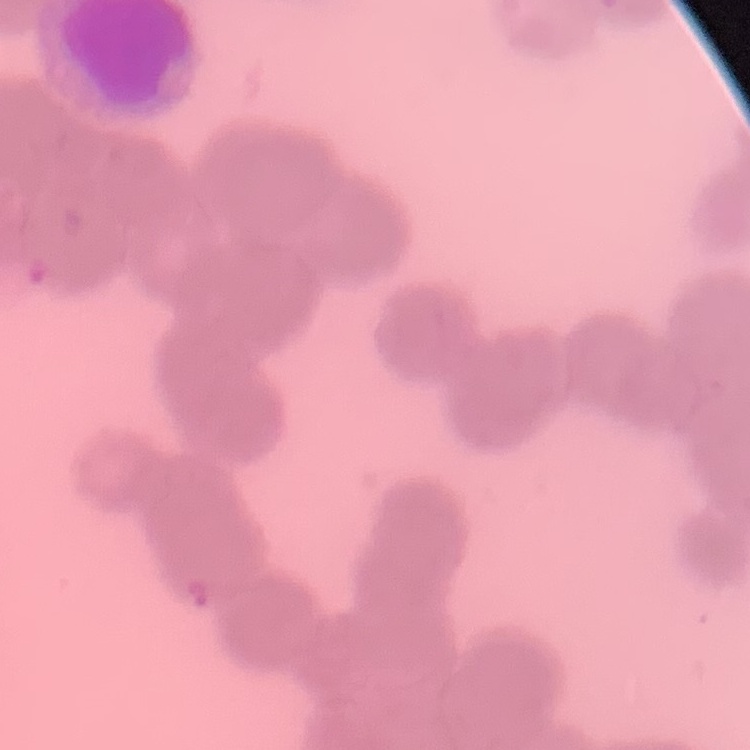

Summary:
  - Red blood cell morphology: rouleaux formation
  - Image type: one tile cut from a larger photomicrograph
  - Stain: Field's or Giemsa
  - Preparation: thin blood film